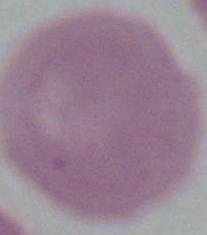
Micrograph. An erythrocyte is seen. 1000x magnification.